Locate every blood parasite and identify its species.
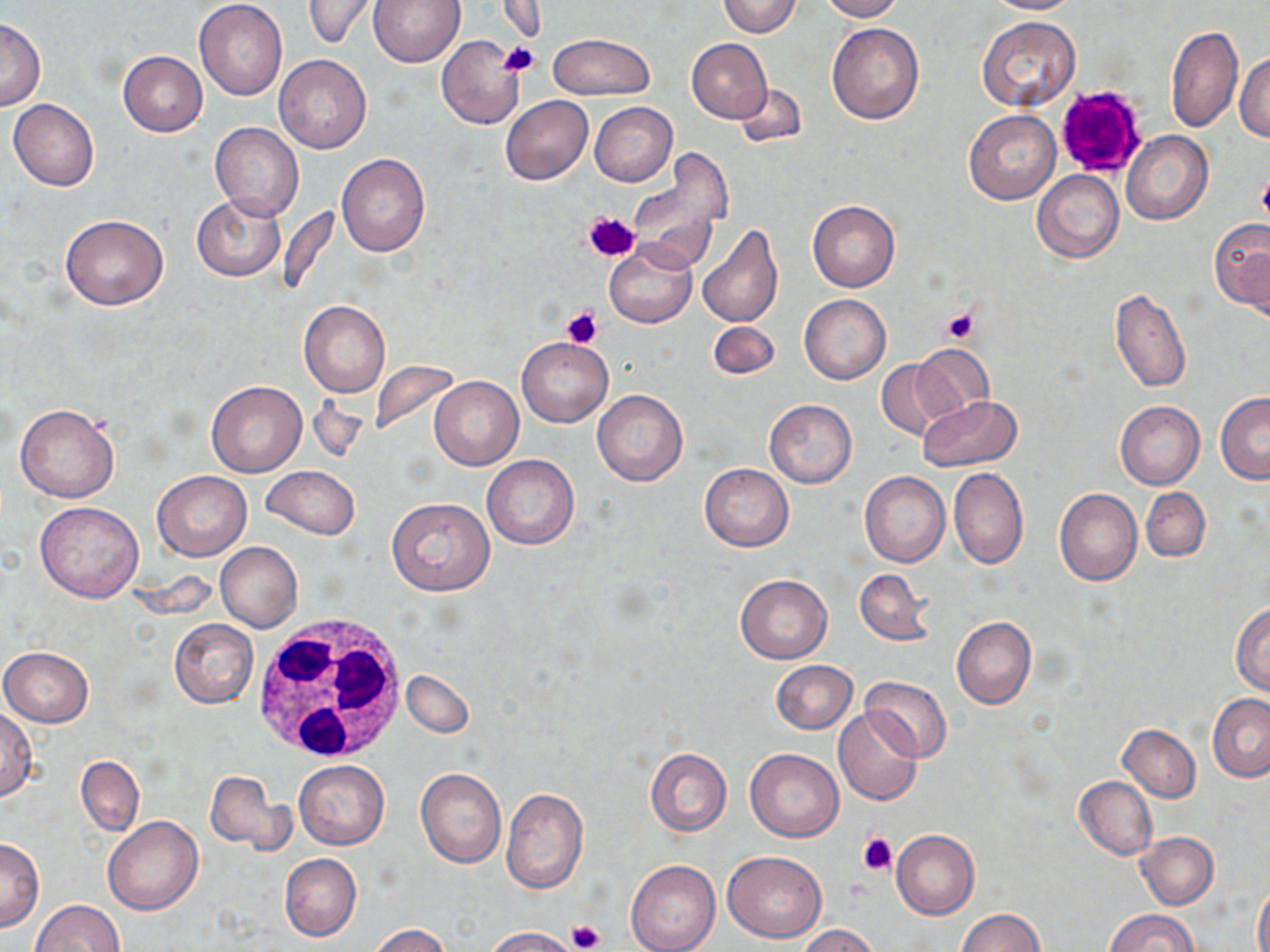
No blood parasites seen.

Approximate bounding boxes as (x1, y1, x2, y2) in pixels. Uninfected red blood cell locations: (368, 0, 464, 67), (718, 0, 803, 36), (819, 0, 901, 21), (984, 0, 1083, 14), (194, 1, 288, 101), (302, 1, 381, 49), (976, 16, 1080, 111), (0, 18, 45, 110), (827, 22, 924, 124), (1166, 24, 1241, 131), (547, 33, 655, 100), (436, 35, 524, 129), (687, 39, 772, 122), (117, 50, 207, 135), (1235, 52, 1270, 144), (274, 54, 371, 154), (732, 81, 807, 148), (500, 96, 592, 184), (8, 98, 99, 191), (590, 102, 676, 186), (963, 109, 1060, 204), (210, 122, 304, 221), (1122, 132, 1212, 225), (626, 148, 734, 274), (336, 153, 430, 256), (1031, 170, 1123, 263), (192, 193, 286, 281), (806, 200, 899, 291), (60, 214, 168, 310), (1210, 217, 1270, 316), (696, 223, 783, 327), (605, 241, 697, 328), (1111, 287, 1190, 394), (799, 294, 891, 384), (298, 300, 390, 398), (707, 320, 779, 379), (517, 337, 613, 426), (911, 343, 994, 419), (876, 360, 950, 441), (430, 376, 522, 470), (206, 380, 306, 476), (592, 389, 688, 486), (1218, 392, 1269, 483), (918, 397, 1021, 472), (764, 400, 857, 487), (1115, 400, 1204, 489), (15, 403, 119, 502), (482, 454, 579, 550), (700, 463, 793, 551), (262, 466, 359, 538), (948, 467, 1028, 569), (151, 469, 250, 561), (860, 471, 950, 567), (1141, 487, 1209, 563), (1055, 488, 1142, 586), (385, 497, 495, 597), (36, 501, 143, 601), (215, 542, 303, 632), (855, 568, 934, 647), (734, 574, 832, 664), (1231, 603, 1270, 695), (951, 616, 1036, 709), (169, 618, 258, 707), (0, 647, 94, 727), (771, 660, 858, 733), (402, 669, 474, 737), (861, 674, 951, 762), (1208, 692, 1270, 782), (0, 707, 38, 801), (833, 709, 922, 806), (1118, 724, 1200, 801), (644, 747, 731, 834), (745, 748, 843, 842), (76, 756, 145, 836), (294, 760, 389, 849), (416, 768, 507, 868), (205, 769, 291, 856), (1074, 776, 1156, 859), (501, 788, 588, 893), (103, 815, 203, 915), (892, 829, 979, 919), (1136, 832, 1218, 909), (0, 838, 44, 931), (723, 849, 826, 943), (280, 853, 360, 942), (626, 859, 718, 952), (1254, 877, 1270, 952), (28, 899, 124, 952), (956, 908, 1045, 952), (1105, 908, 1197, 952), (369, 924, 452, 952), (798, 925, 881, 952), (484, 926, 580, 952). White blood cell locations: (246, 613, 406, 764). Platelet locations: (500, 43, 540, 77), (1053, 84, 1149, 176), (1257, 172, 1270, 225), (584, 209, 640, 261), (562, 306, 602, 349), (941, 307, 980, 344), (858, 832, 898, 873), (566, 919, 604, 952). Slide-level diagnosis: negative for blood parasites. Captured at 1000x magnification. Image is 1270×952 pixels. One field of a larger specimen. May-Grünwald-Giemsa-stained preparation. Thin blood film. Optical microscopy.